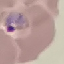
Malaria status: parasitized. Giemsa-stained preparation. Photographed with a smartphone camera at the microscope eyepiece. Thin blood film. Cell patch, automatically extracted from a larger field of view and resized to 64 × 64 pixels.